Locate every leukocyte (white blood cell).
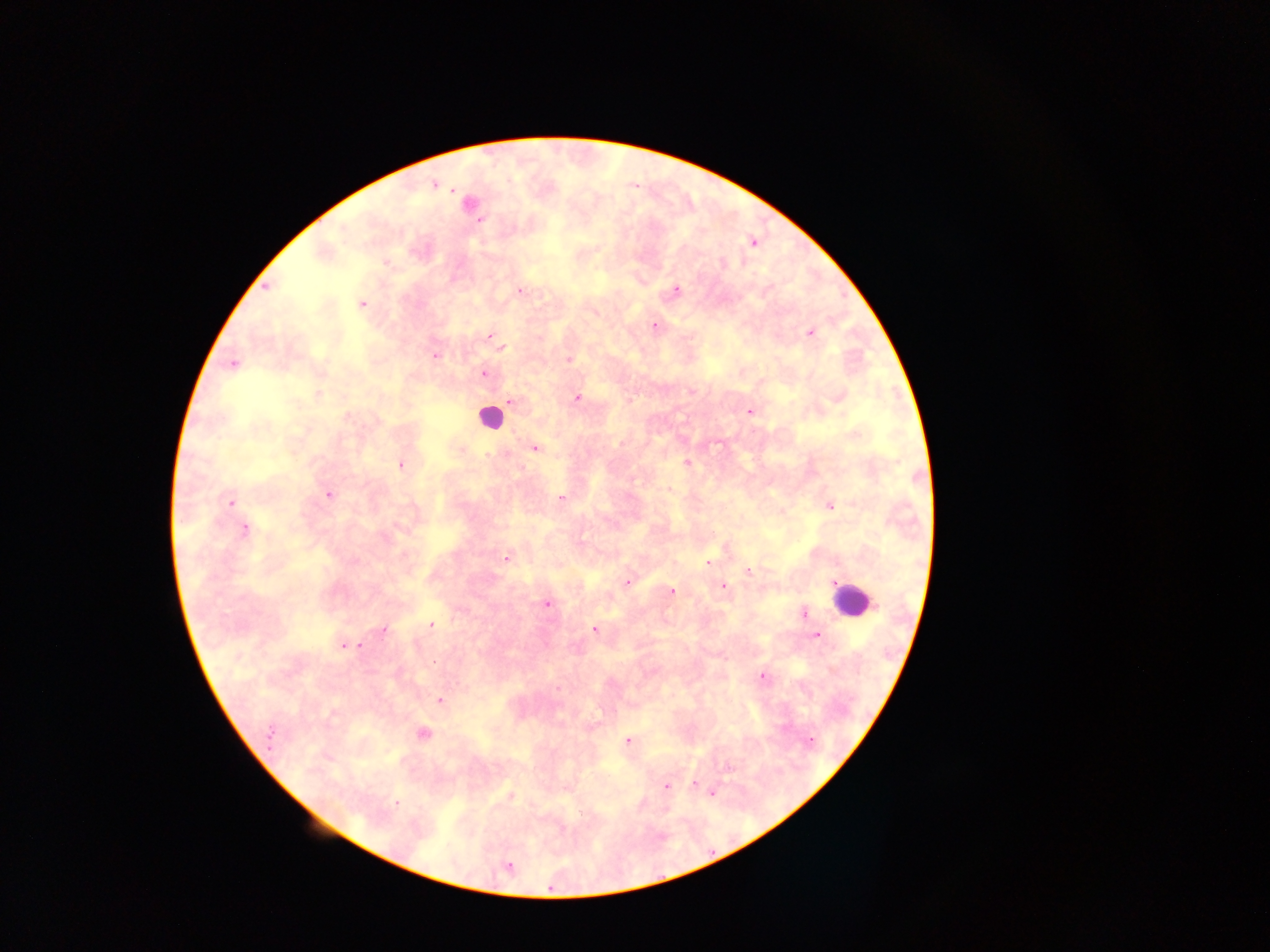

Approximate centers as (x, y) in pixels.
Leukocytes: (489, 418), (851, 598).

capture = mobile-phone photograph through a microscope
field of view = single
preparation = thick blood film
Plasmodium parasite locations = approximate centers as (x, y) in pixels: (434, 185), (480, 221), (753, 244), (386, 263), (267, 287), (677, 290), (520, 291), (362, 304), (654, 326), (811, 333), (490, 336), (500, 346), (435, 356), (569, 359), (233, 364), (484, 374), (691, 390), (317, 395), (577, 397), (509, 401), (749, 412), (535, 448), (686, 462), (400, 465), (669, 489), (328, 494), (560, 499), (231, 502), (830, 506), (244, 528), (507, 558), (708, 562), (749, 571), (627, 581), (723, 586), (672, 591), (547, 604), (803, 613), (431, 625), (383, 629), (594, 629), (816, 635), (344, 645), (359, 646), (763, 676), (439, 700), (423, 734), (269, 736), (811, 740), (627, 741), (728, 768), (693, 784), (666, 786), (510, 794), (712, 794), (397, 803), (508, 866)
country = Ghana
image size = 1270×952 pixels